Classify this cell by malaria status.
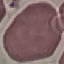

It is uninfected.

Giemsa-stained preparation. Automatically extracted cell patch, resized to 64 × 64 pixels. Acquired by smartphone through the microscope eyepiece. Thin blood smear.